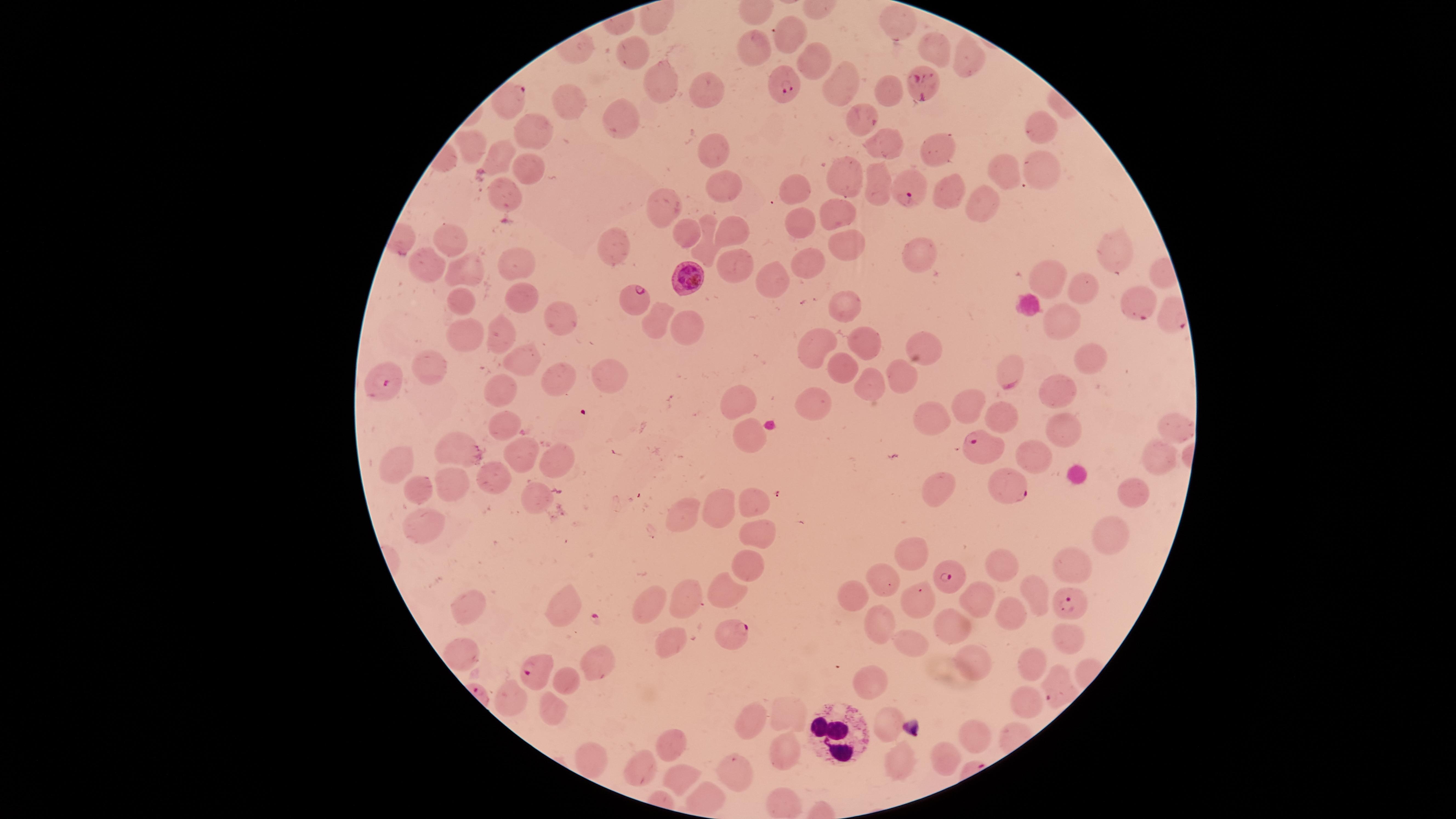
preparation = thin blood smear
visible region = circular
species = Plasmodium falciparum
field of view = single
capture = smartphone photograph through the microscope eyepiece
stain = Giemsa
parasitized red blood cells = approximate marker points as [x, y] in pixels: [919, 81], [784, 84], [507, 98], [910, 188], [687, 277], [633, 298], [1135, 305], [387, 381], [982, 445], [1004, 487], [952, 578], [1067, 599], [737, 632], [538, 673], [1056, 690]
white blood cells = approximate marker points as [x, y] in pixels: [838, 729]
uninfected red blood cells = approximate marker points as [x, y] in pixels: [903, 20], [654, 22], [793, 38], [939, 47], [635, 48], [749, 48], [972, 57], [812, 59], [662, 80], [836, 82], [702, 87], [889, 91], [573, 100], [625, 112], [859, 112], [1039, 126], [535, 131], [886, 140], [706, 144], [477, 145], [942, 151], [504, 156], [1036, 164], [530, 166], [1000, 166], [843, 174], [724, 180], [881, 184], [800, 186], [945, 189], [499, 190], [978, 201], [660, 205], [840, 206], [800, 221], [730, 229], [449, 236], [837, 236], [687, 240], [613, 245], [704, 249], [918, 253], [1118, 253], [804, 262], [522, 263], [426, 265], [731, 265], [463, 271], [777, 275], [1051, 278], [1085, 285], [527, 294], [457, 297], [846, 304], [560, 311], [653, 317], [1062, 325], [684, 329], [460, 337], [499, 338], [866, 343], [820, 344], [922, 346], [1088, 358], [840, 362], [431, 365], [606, 365], [516, 366], [1010, 371], [902, 378], [562, 379], [867, 382], [1059, 388], [742, 394], [500, 395], [968, 402], [808, 404], [933, 411], [1002, 418], [1054, 422], [507, 425], [1168, 426], [749, 436], [527, 451], [461, 452], [1033, 454], [1158, 461], [559, 463], [401, 468], [496, 477], [942, 484], [411, 491], [450, 491], [1133, 491], [530, 494], [758, 502], [721, 507], [689, 508], [418, 526], [750, 530], [1107, 542], [915, 549], [1072, 563], [999, 564], [750, 567], [887, 576], [726, 588], [862, 592], [1036, 592], [689, 594], [924, 596], [977, 599], [652, 603], [468, 605], [568, 606], [1014, 612], [955, 623], [875, 631], [1066, 637], [664, 638], [915, 645], [462, 656], [603, 656], [969, 657], [1032, 666], [568, 678], [865, 685], [515, 700], [552, 704], [1025, 706], [786, 717], [756, 718], [887, 721], [980, 733], [665, 749], [790, 749], [944, 754], [584, 760], [893, 760], [642, 771], [734, 774], [679, 782], [704, 801], [782, 801]
presence = malaria parasites seen
image size = 1456×819 pixels